Report the malaria status of this cell.
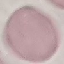

It is uninfected.

Acquired by smartphone through the microscope eyepiece. Giemsa-stained preparation. Automatically extracted cell patch, resized to 64 × 64 pixels. Thin blood smear.